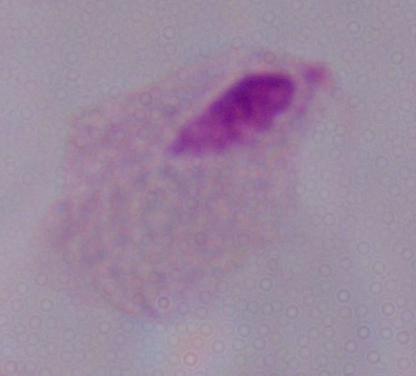

modality = photomicrograph
identification = trichomonad
magnification = 1000x